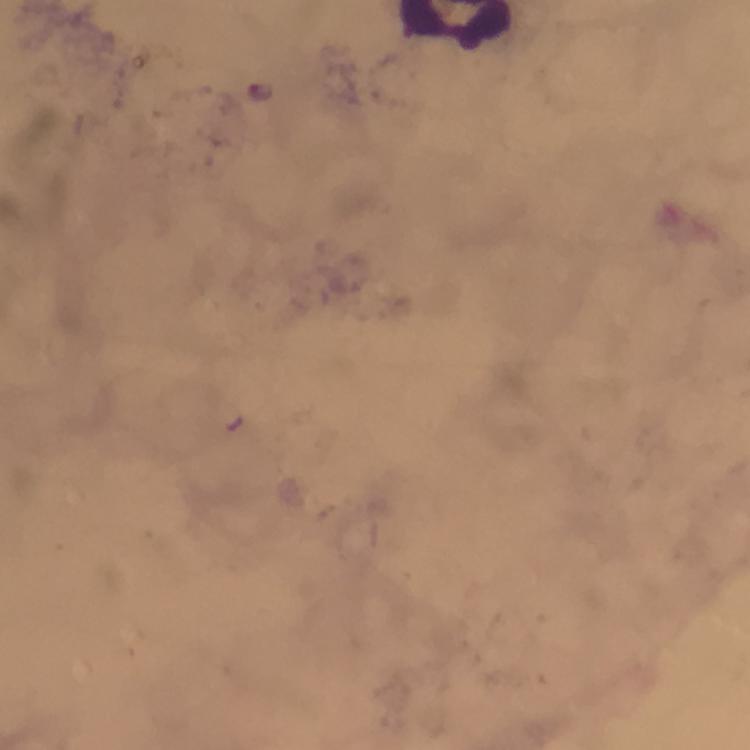
magnification = 100x
cropped from = one field of view
preparation = thick smear
immersion oil = applied
image size = 750×750 pixels
stain = Giemsa
Plasmodium parasite locations = approximate centers as (x, y) in pixels: (261, 89)
context = from a malaria diagnostic workup
capture = smartphone camera through the microscope